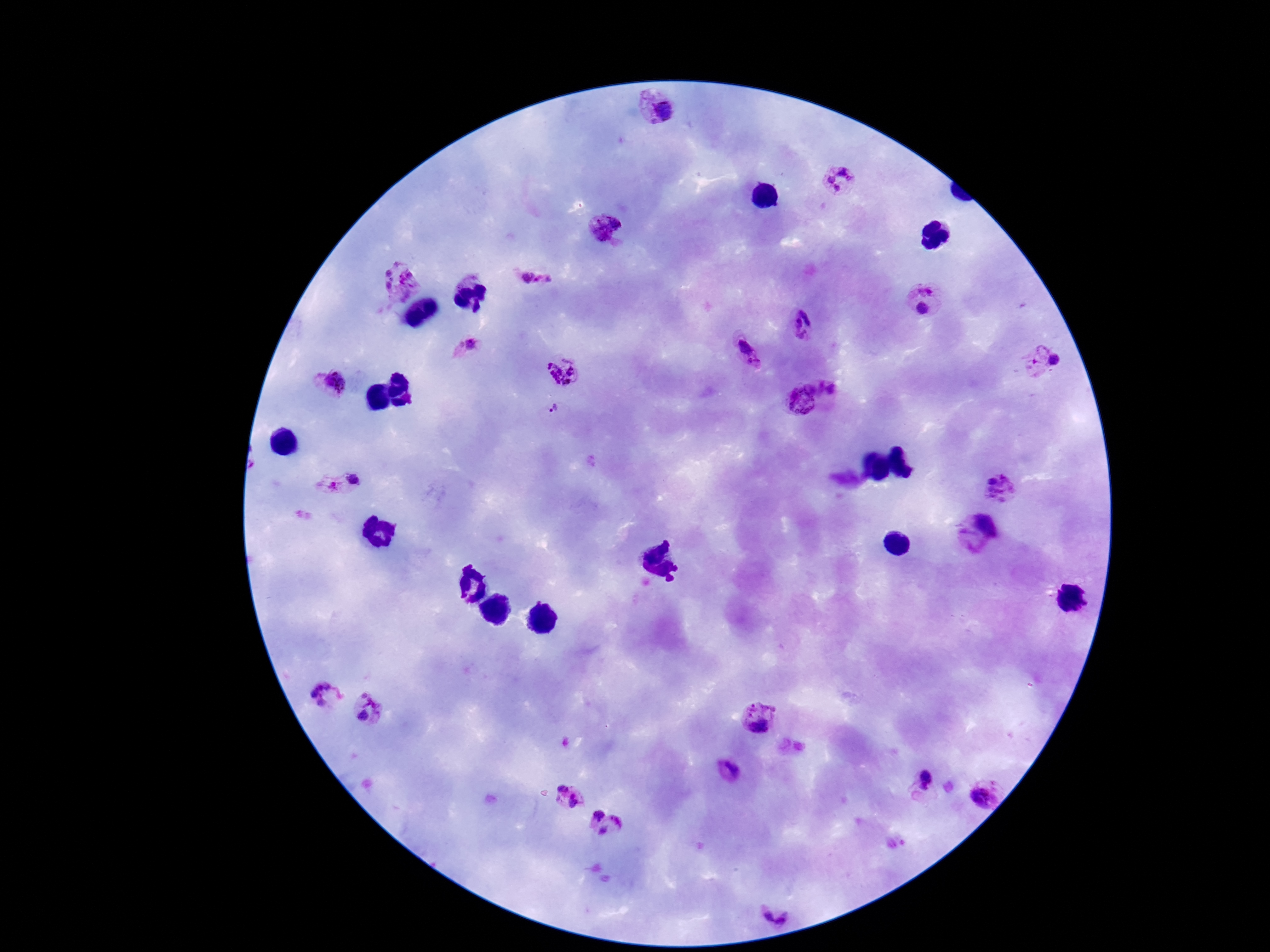

capture = smartphone camera through the microscope eyepiece
image size = 1270×952 pixels
Plasmodium parasite locations = approximate centers as (x, y) in pixels: (655, 107), (841, 183), (606, 227), (537, 278), (398, 281), (927, 284), (923, 308), (808, 328), (472, 348), (749, 354), (1039, 361), (564, 369), (329, 387), (811, 394), (555, 410), (339, 485), (1001, 486), (976, 534), (325, 696), (369, 709), (760, 720), (734, 775), (927, 781), (987, 792), (569, 796), (598, 815), (619, 820), (603, 830), (772, 916)
patient malaria status = positive
magnification = 100x
stain = Giemsa
preparation = thick peripheral-blood smear
field of view = one from this slide